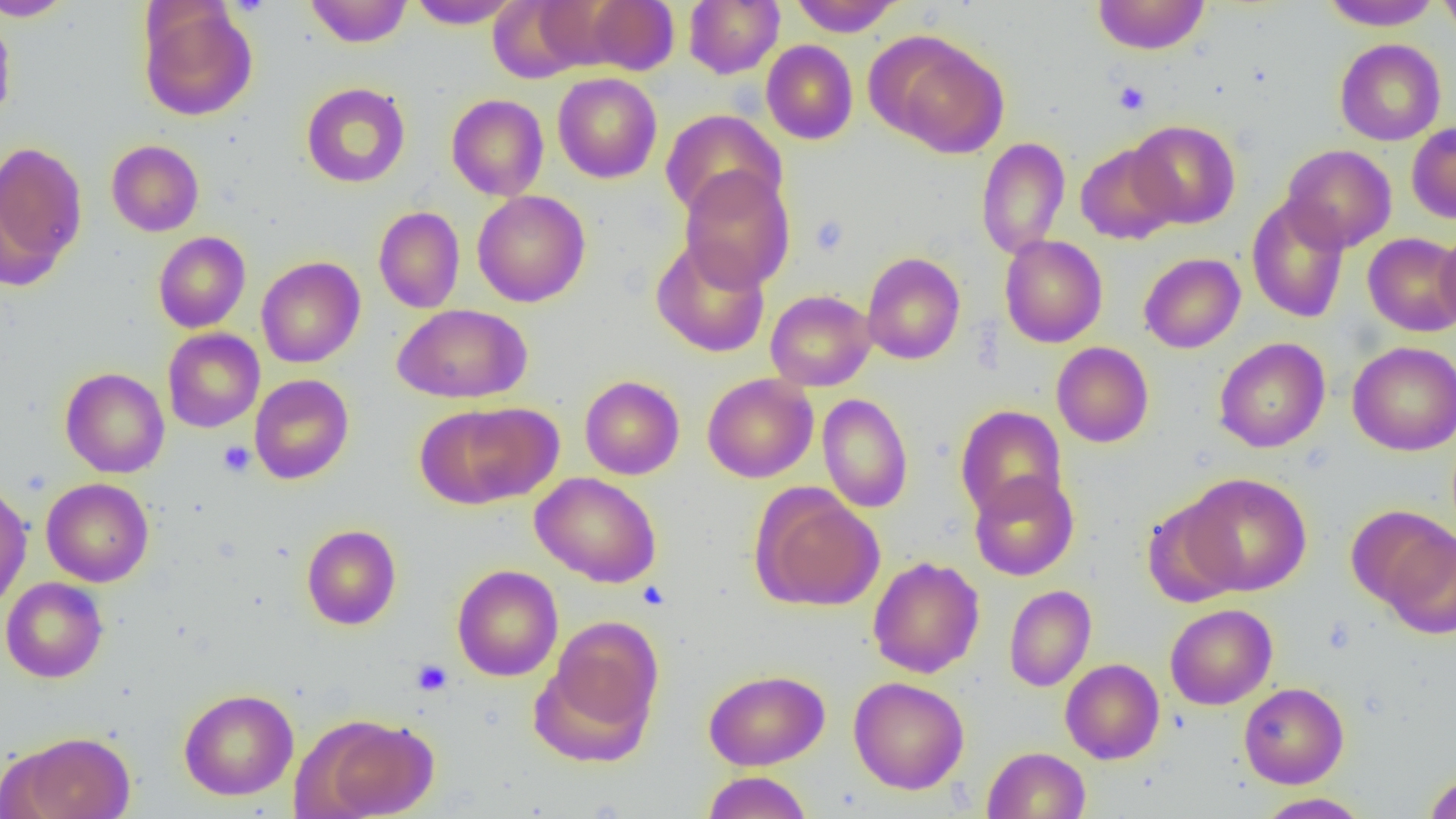 Approximate bounding boxes as (x1, y1, x2, y2) in pixels. Platelet locations: (1113, 80, 1151, 115), (808, 215, 849, 257), (218, 440, 255, 477), (637, 582, 670, 610), (411, 659, 453, 696). Uninfected red blood cell locations: (0, 0, 75, 21), (305, 0, 412, 48), (407, 0, 521, 29), (684, 0, 784, 78), (790, 0, 904, 36), (1092, 0, 1211, 55), (1321, 0, 1442, 31), (1437, 0, 1456, 43), (489, 1, 594, 81), (579, 1, 680, 75), (138, 3, 257, 121), (0, 12, 16, 126), (879, 34, 1010, 159), (1334, 38, 1447, 145), (761, 40, 858, 145), (552, 73, 662, 183), (301, 82, 410, 188), (446, 94, 549, 201), (660, 110, 786, 221), (1128, 120, 1241, 228), (1407, 121, 1456, 224), (976, 137, 1070, 260), (106, 139, 204, 236), (0, 140, 87, 282), (1075, 143, 1180, 244), (1281, 144, 1397, 252), (679, 166, 796, 291), (472, 191, 590, 307), (1246, 195, 1350, 323), (373, 206, 465, 313), (1435, 227, 1456, 333), (153, 232, 251, 333), (1362, 233, 1456, 337), (1000, 235, 1108, 348), (651, 236, 770, 358), (861, 251, 966, 365), (1138, 253, 1246, 353), (256, 257, 365, 368), (765, 289, 876, 391), (393, 304, 532, 404), (162, 328, 265, 433), (1213, 337, 1330, 453), (1348, 340, 1456, 455), (1051, 341, 1154, 448), (60, 367, 170, 479), (702, 373, 818, 483), (250, 374, 354, 484), (579, 375, 685, 480), (817, 393, 913, 513), (418, 403, 560, 507), (955, 405, 1068, 520), (968, 471, 1079, 581), (531, 472, 662, 587), (1180, 473, 1311, 595), (41, 478, 154, 587), (0, 481, 32, 611), (752, 489, 885, 611), (1142, 499, 1244, 607), (1377, 522, 1456, 638), (301, 524, 401, 630), (868, 555, 984, 678), (452, 564, 563, 681), (0, 577, 108, 683), (1004, 585, 1096, 691), (1165, 603, 1277, 710), (545, 615, 663, 736), (1061, 658, 1164, 764), (703, 669, 829, 770), (849, 676, 969, 794), (1238, 682, 1349, 788), (179, 688, 299, 800), (303, 713, 438, 819), (9, 730, 136, 819), (982, 747, 1090, 818), (702, 771, 813, 819), (1423, 771, 1456, 818), (1255, 793, 1372, 818). Slide-level diagnosis: no evidence of blood parasites. One field of a larger specimen. Captured at 1000x magnification. Optical microscopy. Thin blood smear. Image is 1456×819 pixels.